Give the position of every Plasmodium parasite visible.
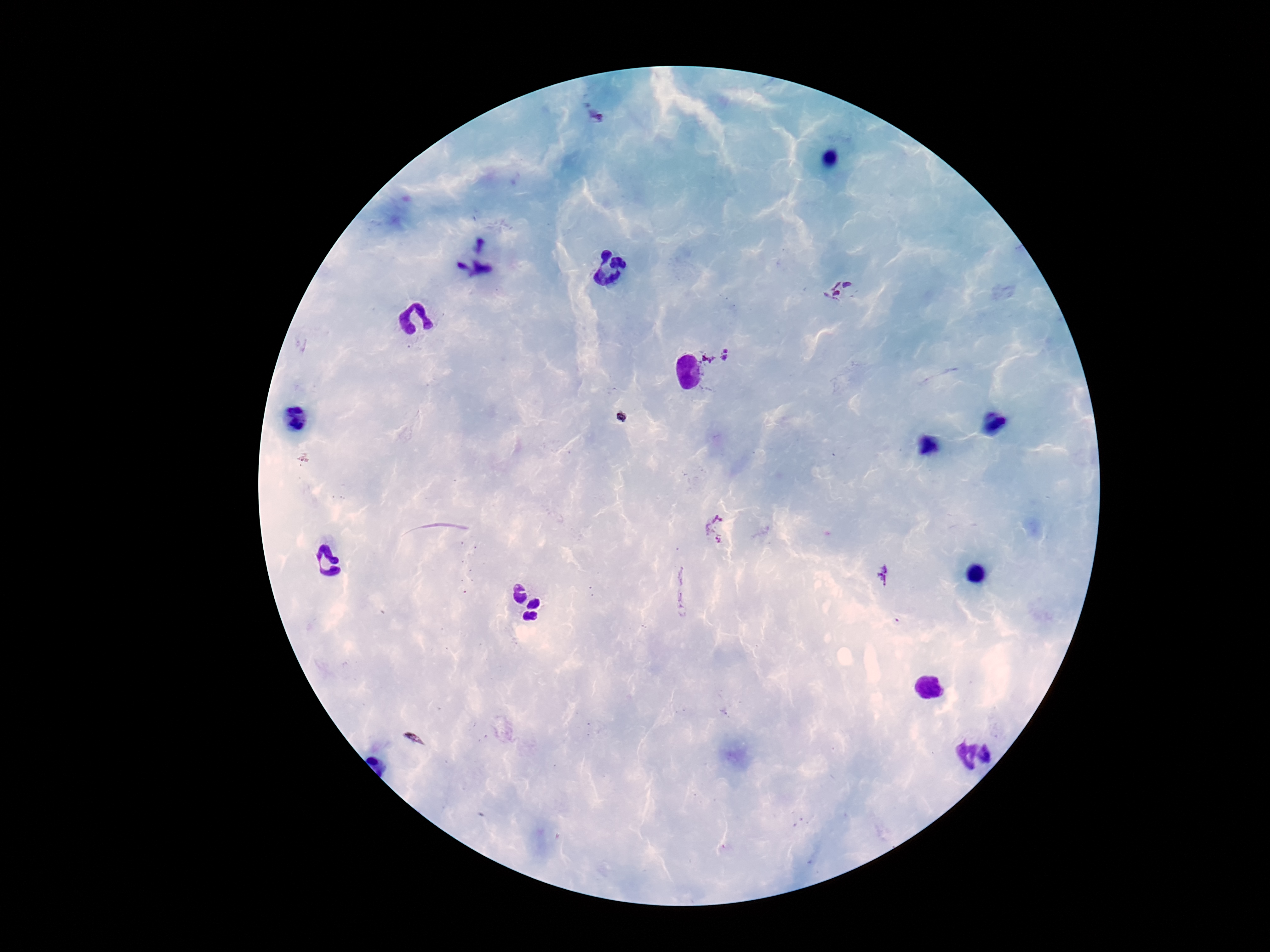

Approximate object centers, in pixels from the top-left corner.
Plasmodium parasites: (x=598, y=113), (x=842, y=290), (x=717, y=355), (x=718, y=528), (x=886, y=577).

Summary:
  - Field of view: single
  - Preparation: thick peripheral-blood smear
  - Magnification: 100x
  - Stain: Giemsa
  - Patient malaria status: infected
  - Capture: smartphone camera through the microscope eyepiece
  - Image size: 1270×952 pixels